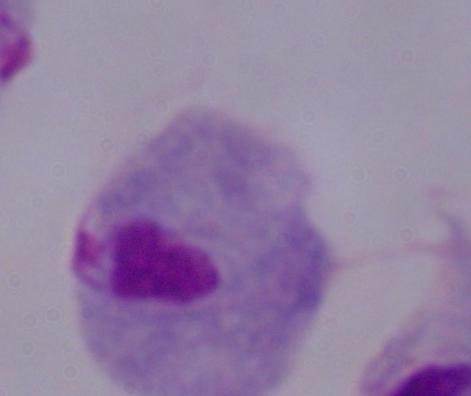
A trichomonad is seen. 1000x magnification. Micrograph.